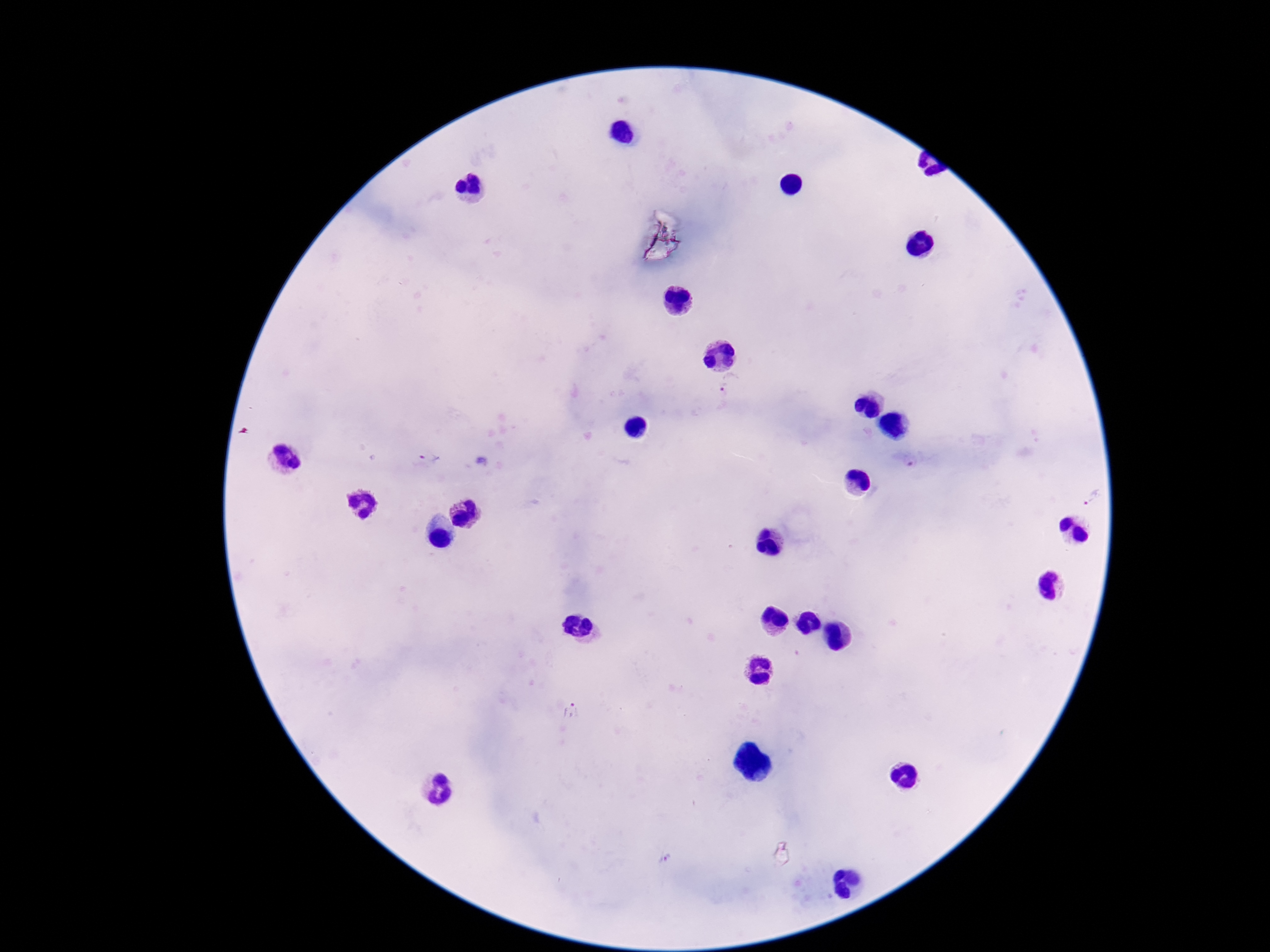

stain = Giemsa
Plasmodium parasite locations = approximate centers as [x, y] in pixels: [732, 386], [428, 458], [1090, 501], [572, 714], [668, 859]
capture = smartphone camera through the microscope eyepiece
field of view = one from this slide
magnification = 100x
preparation = thick blood smear
image size = 1270×952 pixels
patient malaria status = infected